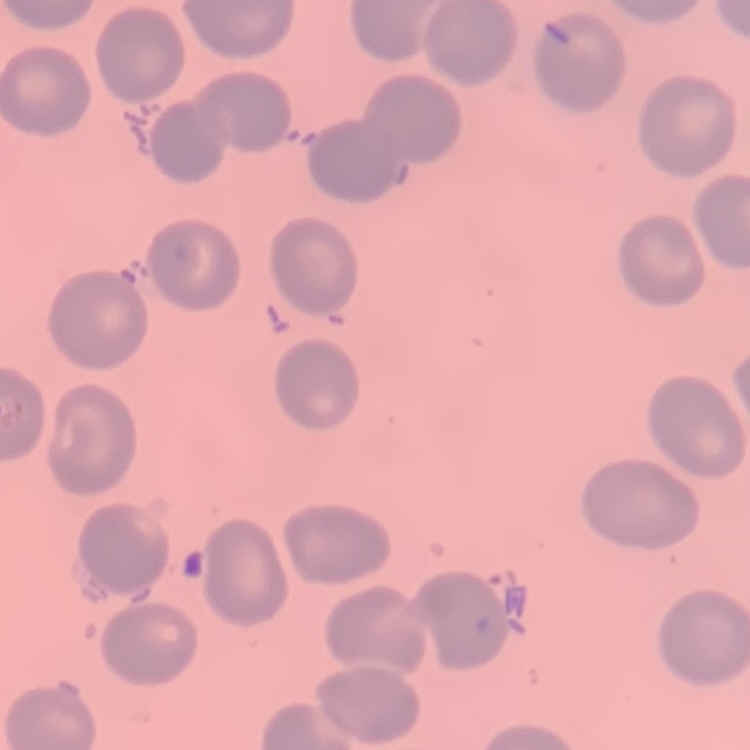

{
  "red_blood_cell_morphology": "no rouleaux formation",
  "preparation": "thin peripheral smear",
  "stain": "Field's or Giemsa",
  "image_type": "square crop of a larger photomicrograph"
}